Point out malaria parasites and leukocytes.
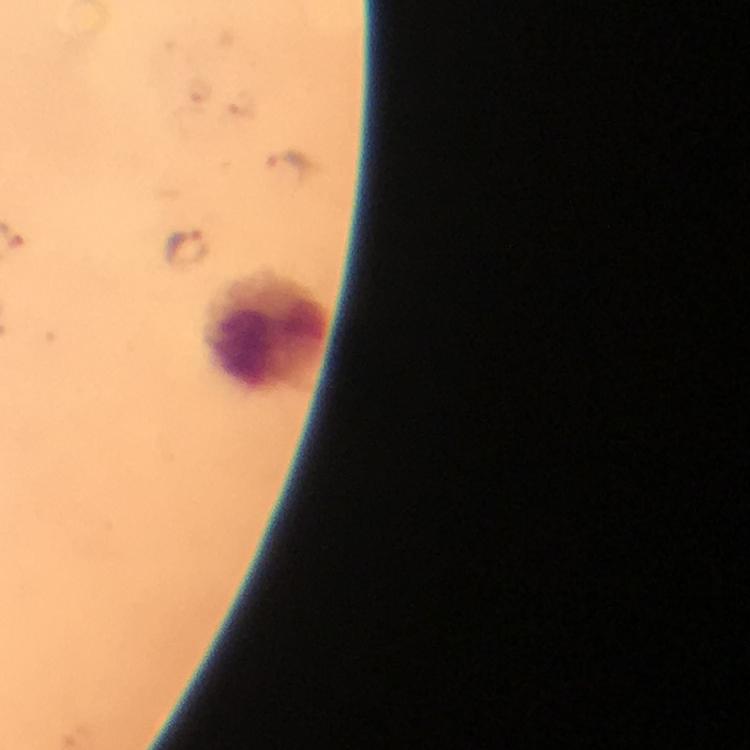

Approximate object centers, in pixels from the top-left corner.
Malaria parasites: (x=284, y=172), (x=185, y=249).
Leukocytes: (x=266, y=332).

Summary:
  - Stain: Giemsa
  - Magnification: 100x
  - Context: from a diagnostic examination for malaria
  - Preparation: thick smear
  - Cropped from: one field of view
  - Immersion oil: applied
  - Capture: smartphone photograph through a microscope
  - Image size: 750×750 pixels